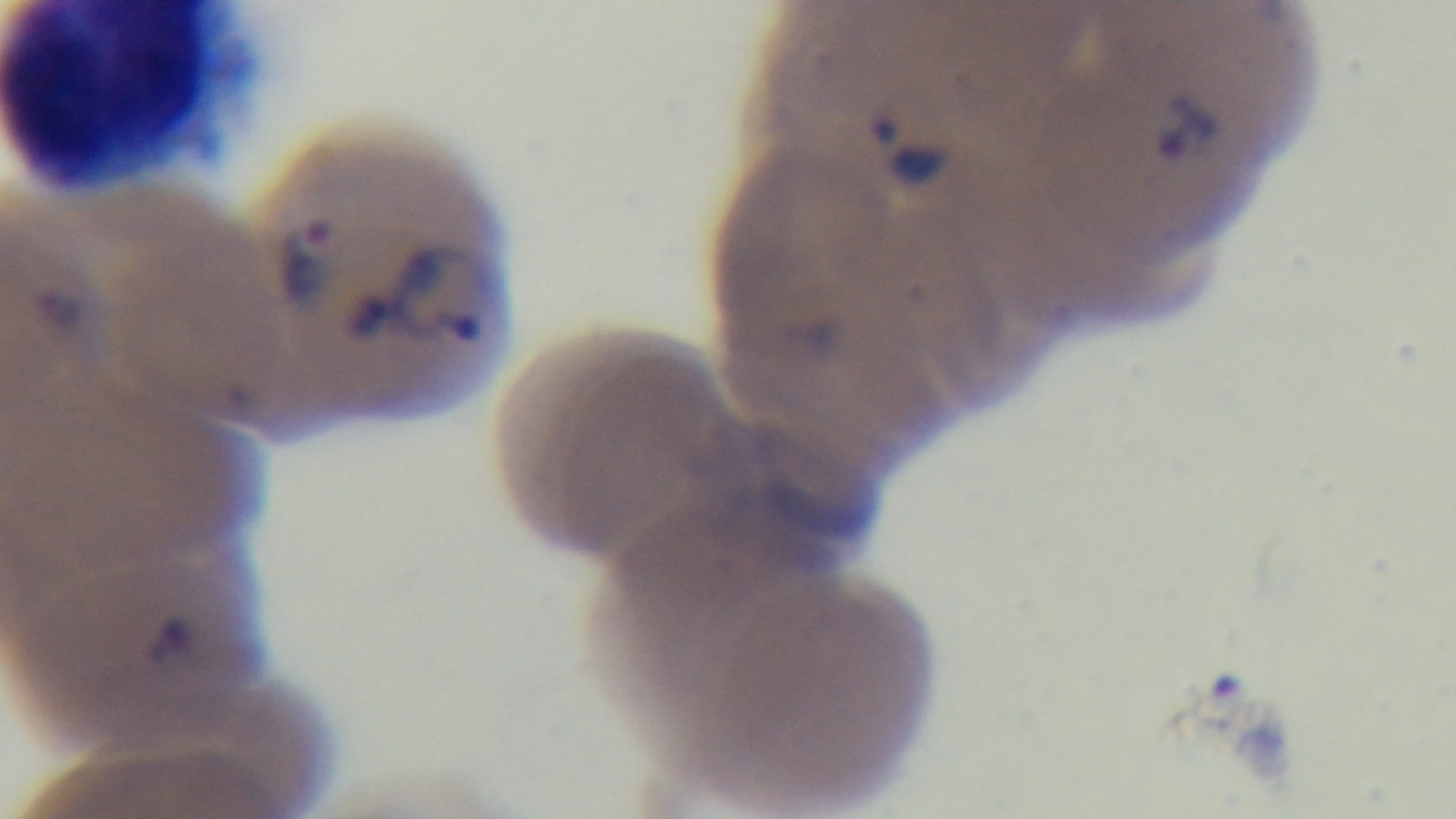
Summary:
  - Capture: mounted 4K digital camera
  - Malaria status: infected
  - Modality: light microscopy
  - Preparation: thin
  - Objective: 100x oil immersion
  - Stain: Giemsa
  - Field of view: one from the slide